Classify this cell by malaria status.
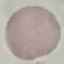
Uninfected.

Summary:
  - Stain: Giemsa
  - Preparation: thin smear
  - Capture: smartphone through the microscope eyepiece
  - Image type: cell patch, automatically extracted from a larger field of view and resized to 64 × 64 pixels